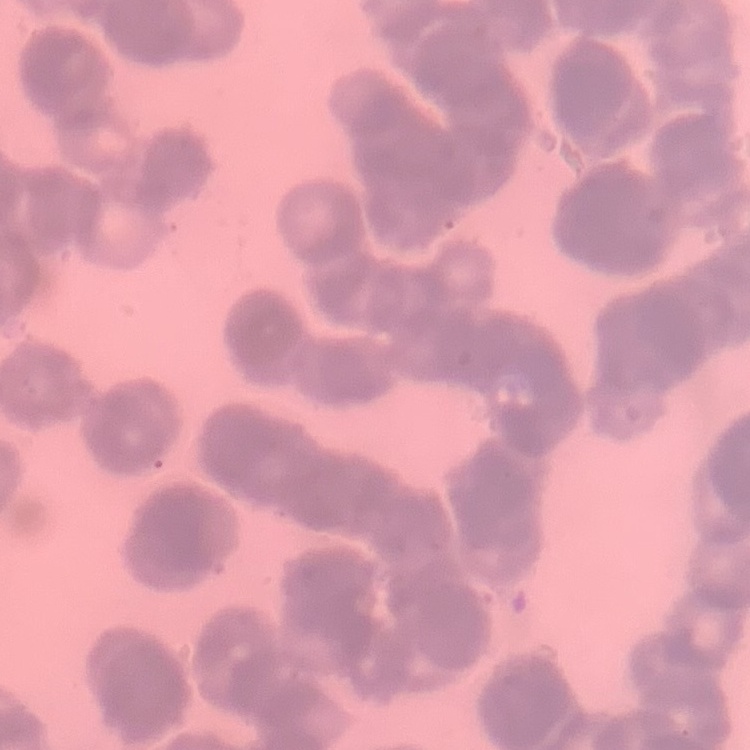
{
  "erythrocyte_morphology": "rouleaux formation",
  "image_type": "one tile cut from a larger photomicrograph",
  "stain": "Field's or Giemsa",
  "preparation": "thin peripheral smear"
}